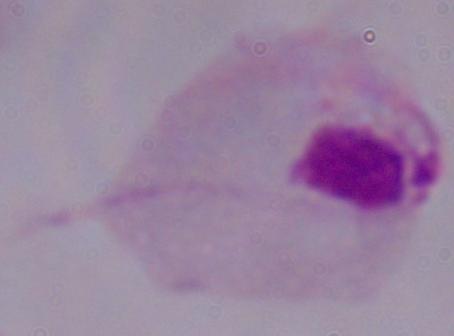
modality = photomicrograph
magnification = 1000x
identification = trichomonad